Describe the morphology of the erythrocytes.
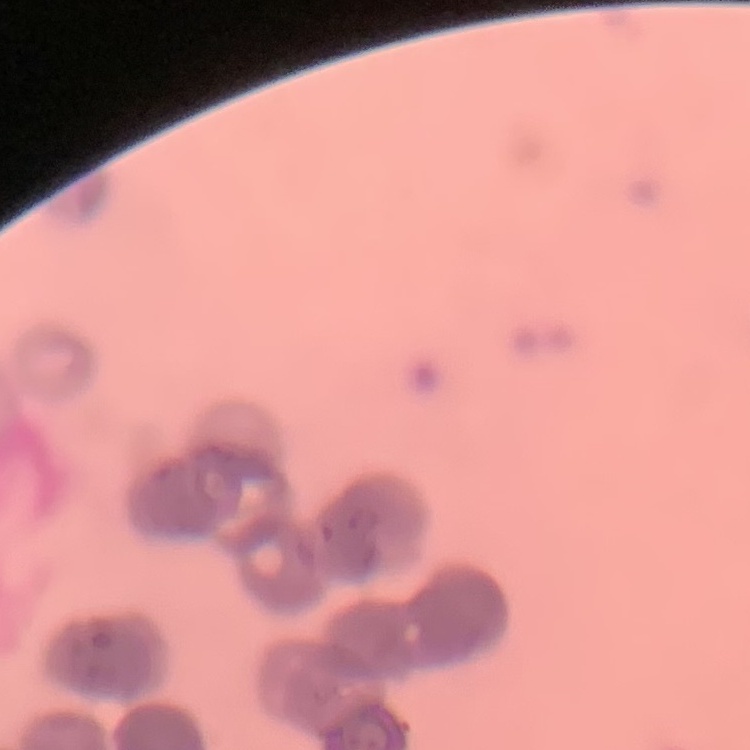
Rouleaux formation.

Summary:
  - Stain: Field's or Giemsa
  - Preparation: thin peripheral smear
  - Image type: square crop of a larger photomicrograph